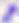 Toxoplasma gondii is shown. Micrograph. 400x magnification.